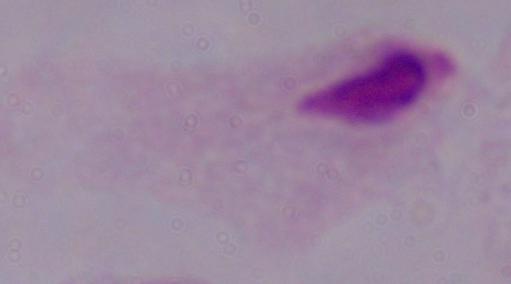
Summary:
  - Identification: trichomonad
  - Modality: micrograph
  - Magnification: 1000x